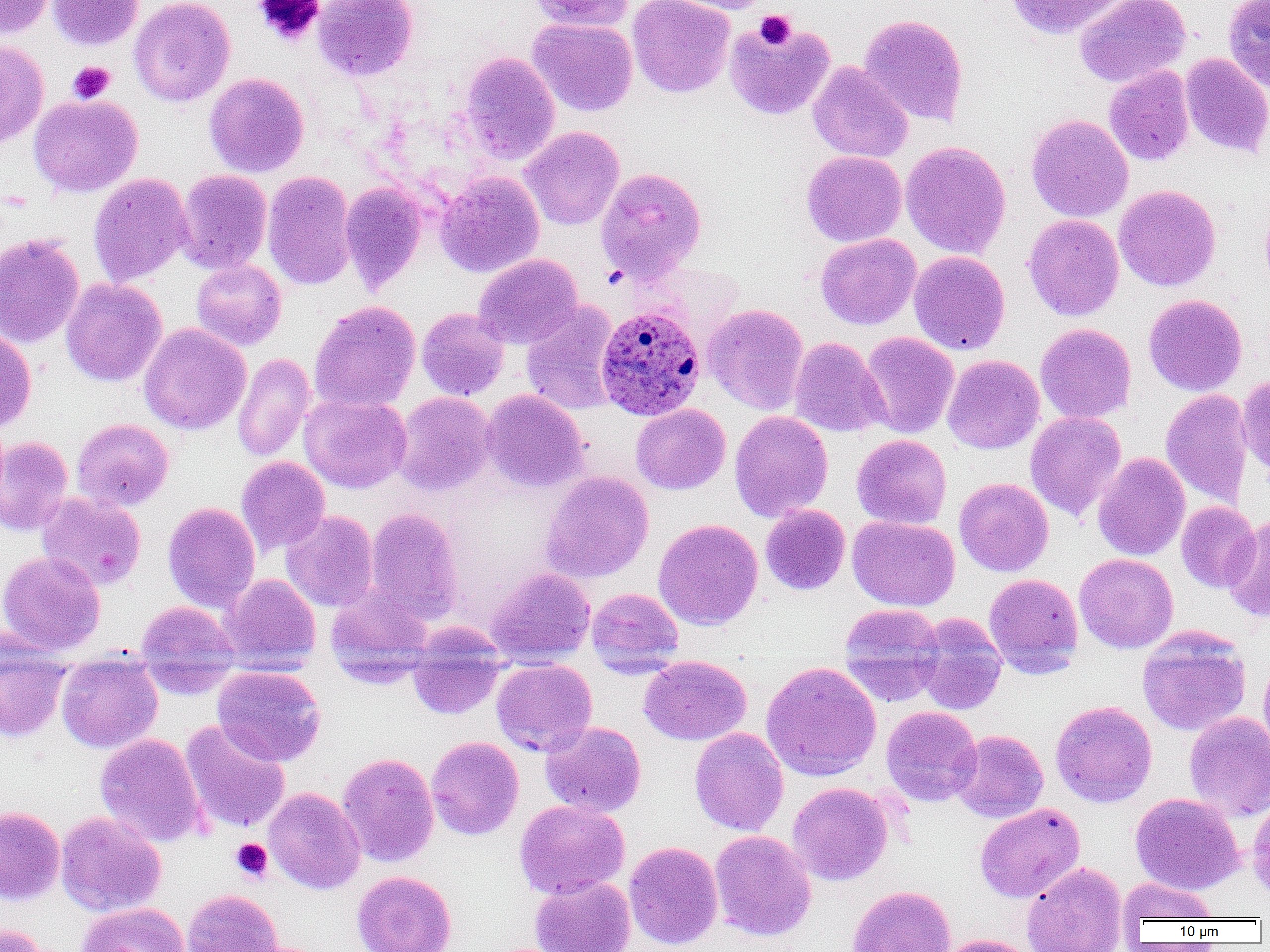
Approximate bounding boxes as named x1/y1/x2/y2 corners in pixels. Plasmodium ovale-infected red blood cell locations: (x1=595, y1=304, x2=705, y2=420). Uninfected red blood cell locations: (x1=0, y1=0, x2=55, y2=38), (x1=47, y1=0, x2=144, y2=51), (x1=129, y1=0, x2=235, y2=106), (x1=313, y1=0, x2=418, y2=81), (x1=529, y1=0, x2=634, y2=32), (x1=627, y1=0, x2=735, y2=98), (x1=664, y1=0, x2=777, y2=14), (x1=1004, y1=0, x2=1128, y2=40), (x1=1074, y1=0, x2=1190, y2=88), (x1=1223, y1=0, x2=1270, y2=93), (x1=859, y1=14, x2=969, y2=126), (x1=527, y1=18, x2=638, y2=117), (x1=724, y1=19, x2=835, y2=120), (x1=0, y1=40, x2=49, y2=148), (x1=459, y1=52, x2=560, y2=164), (x1=1181, y1=54, x2=1270, y2=158), (x1=807, y1=62, x2=914, y2=163), (x1=1103, y1=65, x2=1194, y2=166), (x1=204, y1=73, x2=309, y2=177), (x1=28, y1=94, x2=143, y2=197), (x1=1026, y1=114, x2=1133, y2=222), (x1=519, y1=126, x2=624, y2=230), (x1=900, y1=141, x2=1011, y2=259), (x1=801, y1=150, x2=907, y2=247), (x1=595, y1=167, x2=707, y2=282), (x1=174, y1=169, x2=273, y2=274), (x1=262, y1=171, x2=356, y2=291), (x1=435, y1=172, x2=544, y2=277), (x1=88, y1=173, x2=192, y2=286), (x1=340, y1=181, x2=428, y2=293), (x1=1114, y1=185, x2=1221, y2=291), (x1=1260, y1=202, x2=1270, y2=298), (x1=1023, y1=214, x2=1124, y2=321), (x1=0, y1=233, x2=85, y2=348), (x1=815, y1=233, x2=921, y2=330), (x1=909, y1=250, x2=1010, y2=356), (x1=473, y1=254, x2=582, y2=349), (x1=191, y1=259, x2=287, y2=350), (x1=61, y1=278, x2=166, y2=387), (x1=1144, y1=294, x2=1247, y2=396), (x1=309, y1=301, x2=421, y2=413), (x1=521, y1=302, x2=621, y2=415), (x1=703, y1=304, x2=808, y2=415), (x1=416, y1=307, x2=509, y2=400), (x1=139, y1=323, x2=250, y2=435), (x1=1035, y1=323, x2=1137, y2=424), (x1=0, y1=326, x2=36, y2=432), (x1=859, y1=331, x2=959, y2=438), (x1=789, y1=336, x2=888, y2=438), (x1=232, y1=353, x2=315, y2=462), (x1=942, y1=354, x2=1045, y2=454), (x1=1237, y1=372, x2=1270, y2=480), (x1=1160, y1=388, x2=1254, y2=510), (x1=481, y1=389, x2=589, y2=492), (x1=392, y1=391, x2=495, y2=496), (x1=299, y1=393, x2=412, y2=493), (x1=631, y1=404, x2=730, y2=495), (x1=729, y1=411, x2=833, y2=522), (x1=1025, y1=411, x2=1126, y2=521), (x1=72, y1=418, x2=174, y2=511), (x1=851, y1=434, x2=951, y2=529), (x1=0, y1=436, x2=73, y2=535), (x1=1093, y1=452, x2=1190, y2=561), (x1=236, y1=456, x2=331, y2=555), (x1=541, y1=471, x2=653, y2=583), (x1=954, y1=477, x2=1054, y2=576), (x1=36, y1=492, x2=147, y2=590), (x1=1176, y1=501, x2=1260, y2=592), (x1=162, y1=502, x2=261, y2=613), (x1=760, y1=504, x2=850, y2=595), (x1=364, y1=507, x2=464, y2=624), (x1=280, y1=510, x2=378, y2=612), (x1=847, y1=515, x2=960, y2=611), (x1=1223, y1=515, x2=1270, y2=622), (x1=653, y1=518, x2=763, y2=631), (x1=0, y1=551, x2=105, y2=654), (x1=1075, y1=553, x2=1178, y2=653), (x1=486, y1=567, x2=596, y2=665), (x1=984, y1=573, x2=1083, y2=678), (x1=220, y1=574, x2=320, y2=672), (x1=325, y1=586, x2=433, y2=685), (x1=587, y1=587, x2=683, y2=674), (x1=134, y1=600, x2=240, y2=693), (x1=838, y1=603, x2=944, y2=704), (x1=913, y1=613, x2=1007, y2=714), (x1=407, y1=624, x2=506, y2=720), (x1=1137, y1=628, x2=1251, y2=736), (x1=0, y1=643, x2=70, y2=742), (x1=1258, y1=653, x2=1270, y2=761), (x1=56, y1=654, x2=163, y2=753), (x1=639, y1=655, x2=751, y2=745), (x1=491, y1=658, x2=597, y2=756), (x1=761, y1=661, x2=882, y2=781), (x1=212, y1=665, x2=326, y2=766), (x1=1050, y1=700, x2=1157, y2=807), (x1=881, y1=705, x2=983, y2=806), (x1=1184, y1=711, x2=1270, y2=822), (x1=180, y1=719, x2=291, y2=835), (x1=540, y1=721, x2=647, y2=817), (x1=689, y1=727, x2=789, y2=836), (x1=951, y1=729, x2=1049, y2=822), (x1=95, y1=733, x2=207, y2=848), (x1=426, y1=736, x2=523, y2=840), (x1=337, y1=752, x2=439, y2=867), (x1=787, y1=782, x2=893, y2=885), (x1=263, y1=787, x2=365, y2=894), (x1=1130, y1=793, x2=1245, y2=894), (x1=1247, y1=794, x2=1270, y2=906), (x1=515, y1=799, x2=630, y2=900), (x1=975, y1=802, x2=1085, y2=903), (x1=0, y1=806, x2=64, y2=905), (x1=56, y1=811, x2=166, y2=916), (x1=710, y1=830, x2=816, y2=941), (x1=623, y1=841, x2=723, y2=950), (x1=1021, y1=861, x2=1128, y2=952), (x1=351, y1=870, x2=457, y2=952), (x1=530, y1=876, x2=635, y2=952), (x1=1118, y1=877, x2=1219, y2=923), (x1=847, y1=885, x2=956, y2=952), (x1=181, y1=889, x2=284, y2=952), (x1=76, y1=902, x2=189, y2=952), (x1=0, y1=922, x2=55, y2=952), (x1=937, y1=934, x2=1037, y2=952). Platelet locations: (x1=254, y1=0, x2=325, y2=47), (x1=754, y1=10, x2=796, y2=50), (x1=68, y1=62, x2=115, y2=103), (x1=230, y1=838, x2=273, y2=882). Slide-level diagnosis: Plasmodium ovale. Light microscopy. Thin blood film. Image is 1270×952 pixels. One field of a larger specimen. Captured at 1000x magnification.